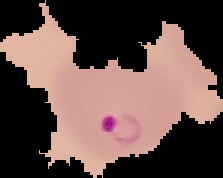
result = malaria parasites detected
image type = segmented cell region with the area outside set to black
preparation = thin blood film
image size = 223×178 pixels